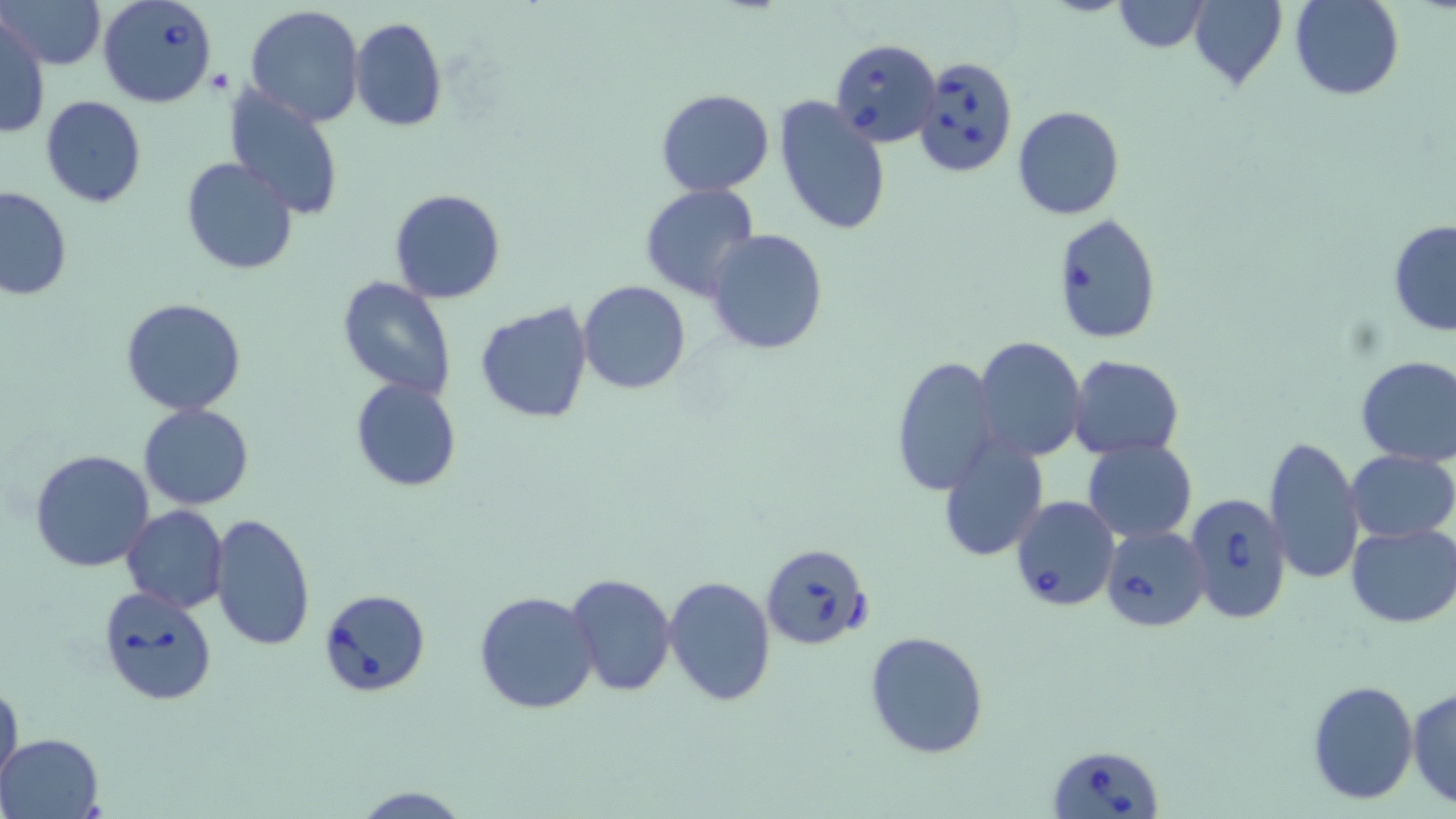

Babesia divergens-infected red blood cell locations = approximate bounding boxes as [x1, y1, x2, y2] in pixels: [97, 0, 220, 108], [830, 37, 941, 149], [916, 54, 1017, 178], [1183, 492, 1294, 625], [1010, 496, 1120, 612], [1102, 525, 1210, 632], [761, 542, 873, 652], [96, 584, 216, 706], [319, 587, 432, 699], [1047, 745, 1163, 819]
slide-level diagnosis = Babesia divergens
preparation = thin blood film
magnification = 1000x
field of view = one of a larger specimen
stain = May-Grünwald-Giemsa
modality = light microscopy
image size = 1456×819 pixels
uninfected red blood cell locations = approximate bounding boxes as [x1, y1, x2, y2] in pixels: [2, 0, 104, 69], [1189, 0, 1287, 89], [1290, 0, 1403, 100], [1114, 1, 1210, 53], [244, 5, 366, 127], [1, 14, 49, 140], [349, 17, 447, 132], [224, 85, 344, 221], [655, 88, 776, 198], [40, 95, 147, 208], [773, 96, 892, 236], [1012, 105, 1125, 219], [181, 156, 300, 275], [640, 183, 761, 300], [0, 186, 73, 302], [389, 188, 506, 304], [1052, 214, 1162, 345], [1388, 219, 1456, 336], [704, 229, 829, 356], [337, 276, 457, 402], [576, 280, 691, 393], [119, 297, 247, 416], [473, 303, 595, 423], [974, 335, 1087, 461], [1066, 354, 1185, 458], [889, 355, 1000, 497], [1355, 356, 1456, 467], [350, 378, 462, 492], [139, 402, 254, 510], [1266, 436, 1365, 587], [937, 437, 1049, 560], [1084, 438, 1197, 544], [30, 449, 156, 573], [1345, 450, 1456, 543], [121, 506, 229, 613], [209, 512, 316, 651], [1346, 524, 1456, 627], [568, 572, 677, 697], [664, 577, 776, 705], [473, 591, 600, 714], [865, 631, 991, 760], [0, 678, 23, 792], [1308, 679, 1418, 804], [1408, 687, 1456, 807], [1, 731, 104, 817], [348, 786, 472, 818]